Point out each Plasmodium parasite.
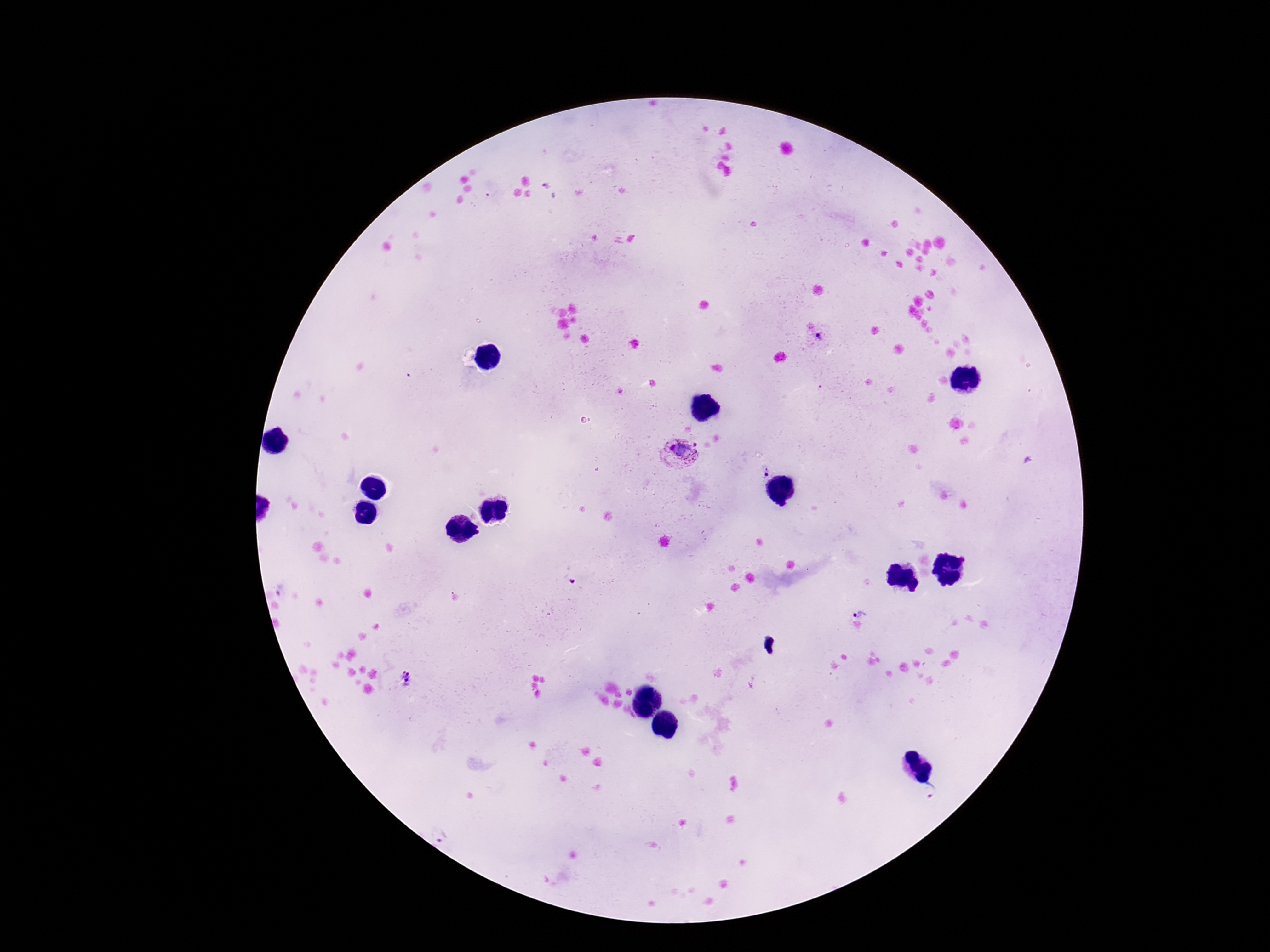

Approximate centers as [x, y] in pixels.
Plasmodium parasites: [821, 339], [680, 455], [765, 472], [283, 591], [861, 612], [406, 677], [931, 793], [445, 836].

preparation: thick blood film
magnification: 100x
stain: Giemsa
image_size: 1270×952 pixels
field_of_view: single
capture: smartphone camera through the microscope eyepiece
patient_malaria_status: positive